Report the malaria status of this cell.
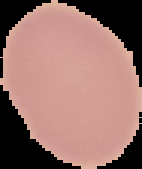
It is uninfected.

image size = 142×169 pixels
preparation = thin blood film
image type = segmented cell region on a black background